Locate every Plasmodium parasite.
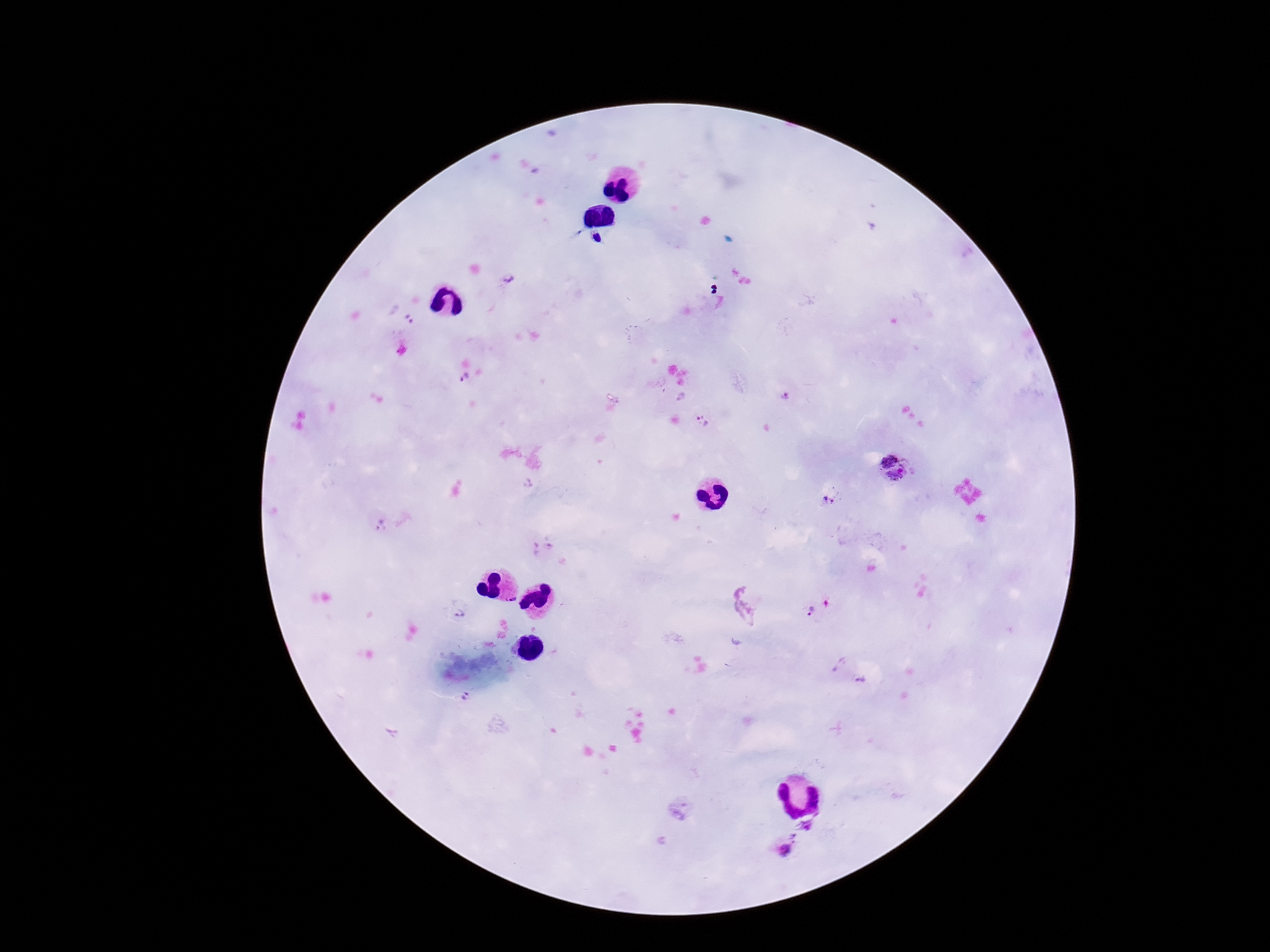

Approximate centers as (x, y) in pixels.
Plasmodium parasites: (509, 278), (410, 319), (464, 378), (785, 397), (703, 422), (886, 452), (898, 477), (829, 502), (812, 611), (461, 614), (838, 664), (861, 680), (464, 698), (808, 825), (784, 850).

field of view = one from this slide
stain = Giemsa
patient malaria status = positive
magnification = 100x
preparation = thick blood smear
capture = smartphone camera through the microscope eyepiece
image size = 1270×952 pixels